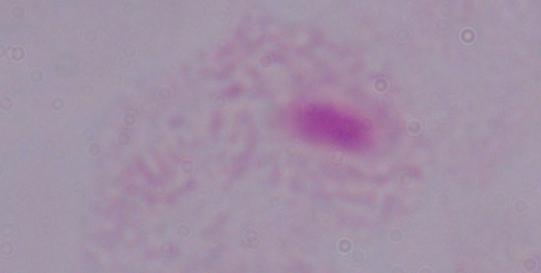
1000x magnification. A trichomonad is shown. Photomicrograph.